Comment on the morphology of the red blood cells.
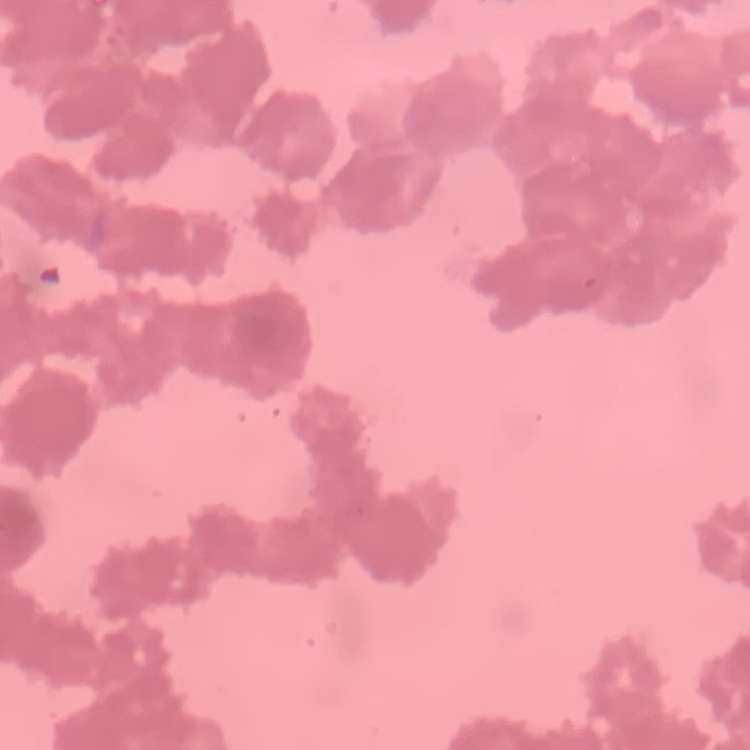

Rouleaux formation.

image_type: one tile cut from a larger photomicrograph
stain: Field's or Giemsa
preparation: thin peripheral smear